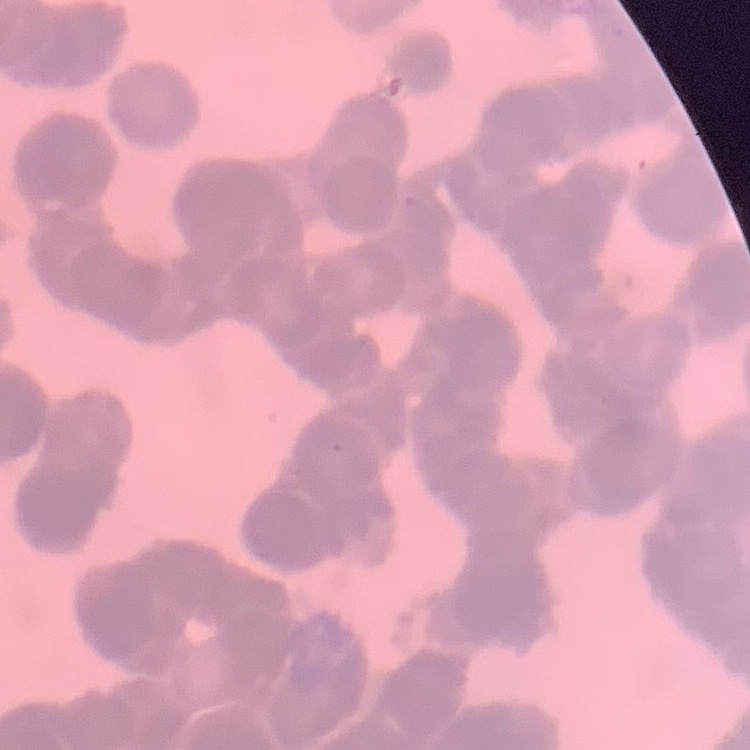

{
  "red_blood_cell_morphology": "rouleaux formation",
  "image_type": "square crop of a larger photomicrograph",
  "stain": "Field's or Giemsa",
  "preparation": "thin blood smear"
}